Identify the cell.
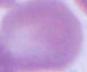

This is an erythrocyte.

Captured at 1000x magnification. Micrograph.